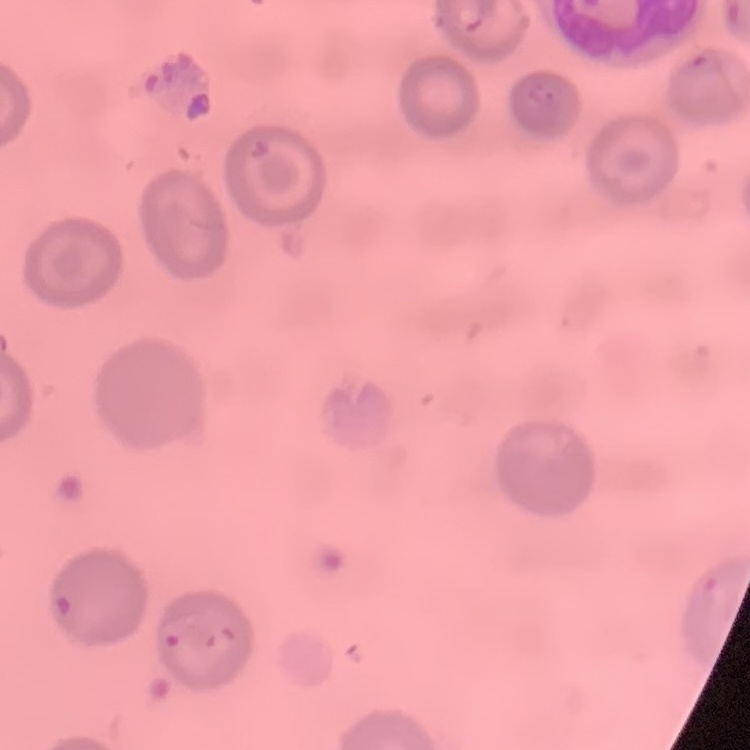
red blood cell morphology = no rouleaux formation
preparation = thin blood film
image type = square crop of a larger photomicrograph
stain = Field's or Giemsa